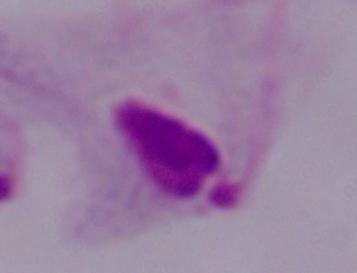

Summary:
  - Modality: photomicrograph
  - Magnification: 1000x
  - Identification: trichomonad